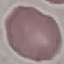

malaria status = uninfected
stain = Giemsa
preparation = thin blood smear
capture = smartphone camera at the microscope eyepiece
image type = cell patch, automatically extracted from a larger field of view and resized to 64 × 64 pixels